Assess this cell for malaria.
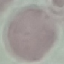

Uninfected.

stain = Giemsa
image type = automatically extracted cell patch, resized to 64 × 64 pixels
capture = smartphone camera at the microscope eyepiece
preparation = thin smear